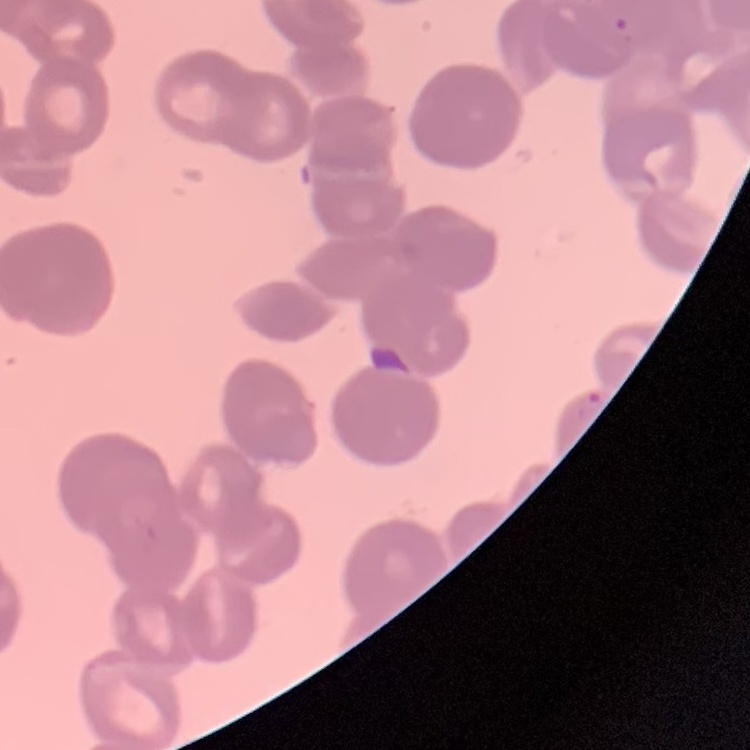

{
  "red_blood_cell_morphology": "rouleaux formation",
  "preparation": "thin blood film",
  "stain": "Field's or Giemsa",
  "image_type": "square crop of a larger photomicrograph"
}